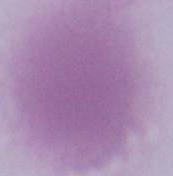
An erythrocyte is seen. Captured at 1000x magnification. Micrograph.